Assess the morphology of the erythrocytes.
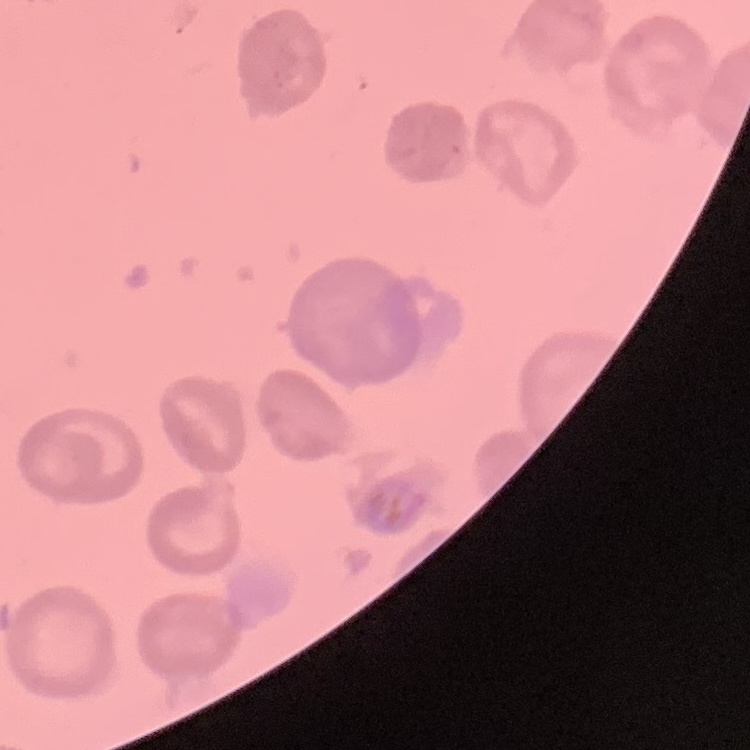
They show no rouleaux formation.

stain = Field's or Giemsa
preparation = thin blood film
image type = one tile cut from a larger photomicrograph